Assess this cell for malaria.
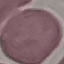

Uninfected.

Summary:
  - Preparation: thin blood film
  - Image type: automatically extracted cell patch, resized to 64 × 64 pixels
  - Stain: Giemsa
  - Capture: smartphone camera at the microscope eyepiece